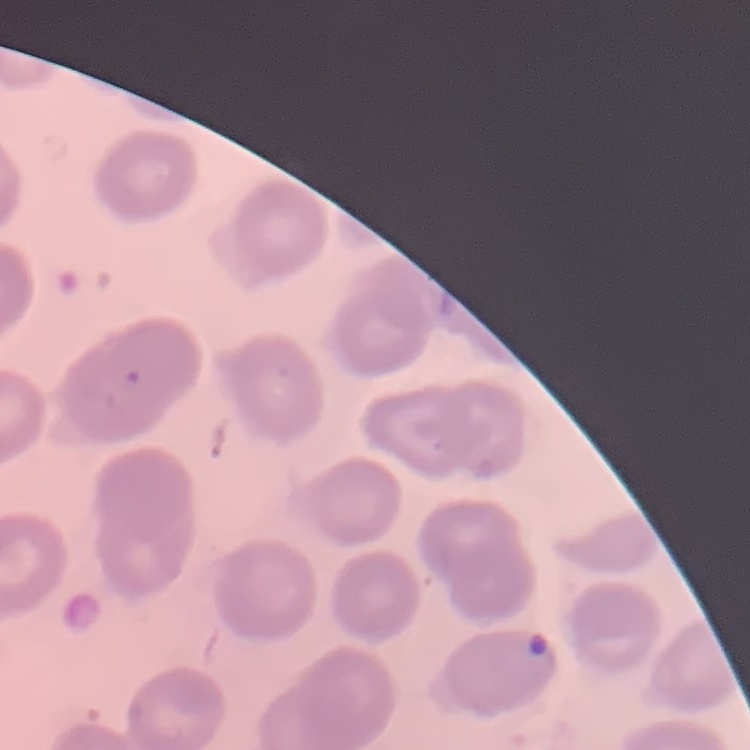

Summary:
  - Erythrocyte morphology: no rouleaux formation
  - Stain: Field's or Giemsa
  - Image type: square crop of a larger photomicrograph
  - Preparation: thin peripheral smear